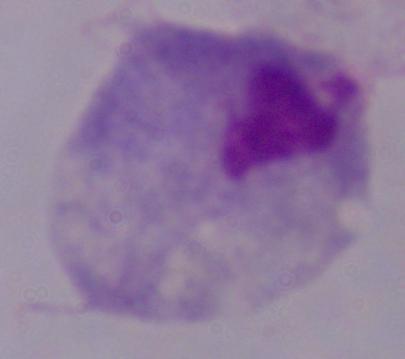 Micrograph. 1000x magnification. A trichomonad is seen.